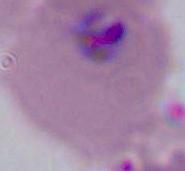

identification = Plasmodium
magnification = 400x or 1000x
modality = micrograph